Classify this cell by malaria status.
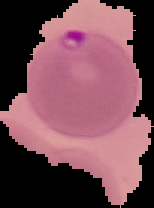
It is parasitized.

image_size: 154×208 pixels
image_type: segmented cell region on a black background
preparation: thin blood smear